Locate every Plasmodium falciparum parasite and give its life-cycle stage, and locate every leukocyte and any debris.
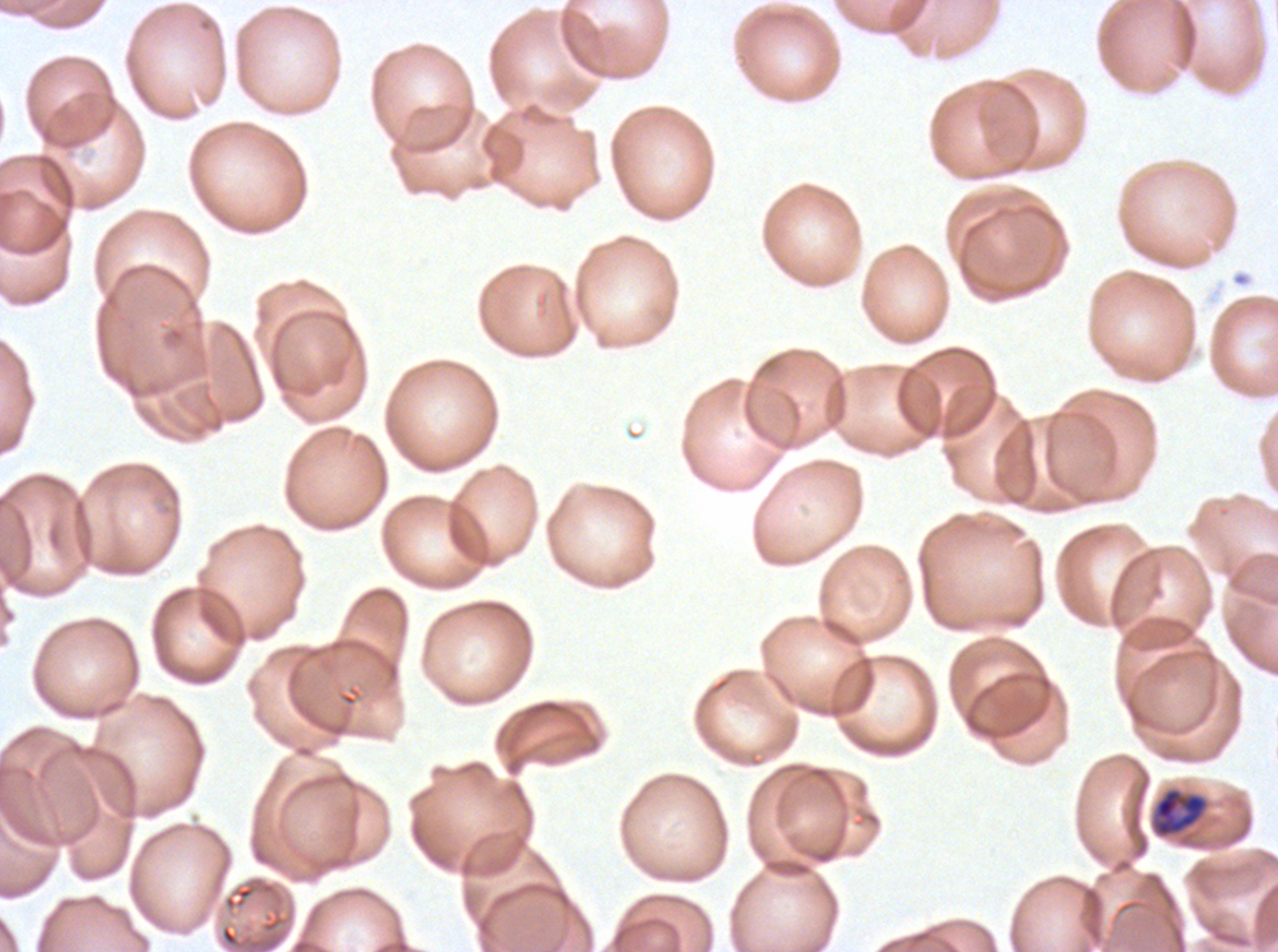

Approximate bounding rectangles given as corner coordinates in pixels from the top-left.
Mid trophozoites: (x1=1153, y1=787, x2=1208, y2=837).
No rings, late-ring/early-trophozoite forms, late trophozoites, early schizonts, late schizonts, segmenters, gametocytes, leukocytes, or debris observed.

Summary:
  - Preparation: thin blood film
  - Specimen: ex-vivo Plasmodium falciparum culture from a patient in The Gambia, grown for 24 to 48 hours
  - Image size: 1278×952 pixels
  - Stain: Giemsa
  - Field of view: one sub-image of a larger composite